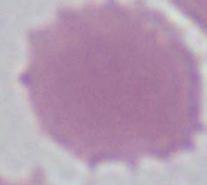
Summary:
  - Identification: erythrocyte
  - Magnification: 1000x
  - Modality: photomicrograph